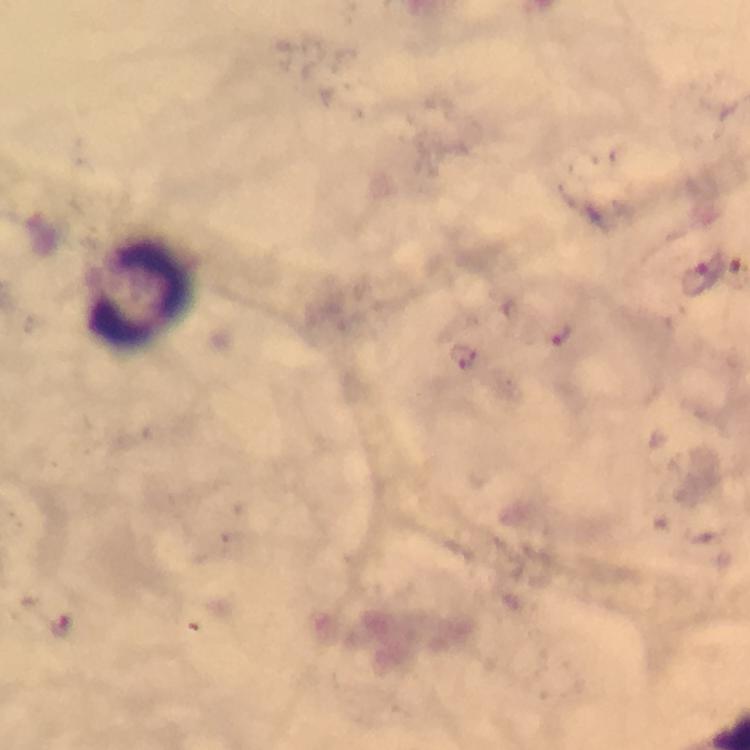
Approximate object centers, in pixels from the top-left corner. Leukocyte locations: (x=142, y=294). Plasmodium parasite locations: (x=705, y=273), (x=563, y=333). At 100x magnification. Thick smear. A crop from one field of view. Photographed through the microscope with a smartphone camera. Giemsa stain. Immersion oil applied. From a diagnostic examination for malaria. Image is 750×750 pixels.